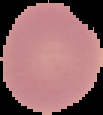

Image is 103×115 pixels. Result: no malaria parasites detected. From a thin blood smear. The area outside the segmented cell region is set to black.